State the blood parasite species.
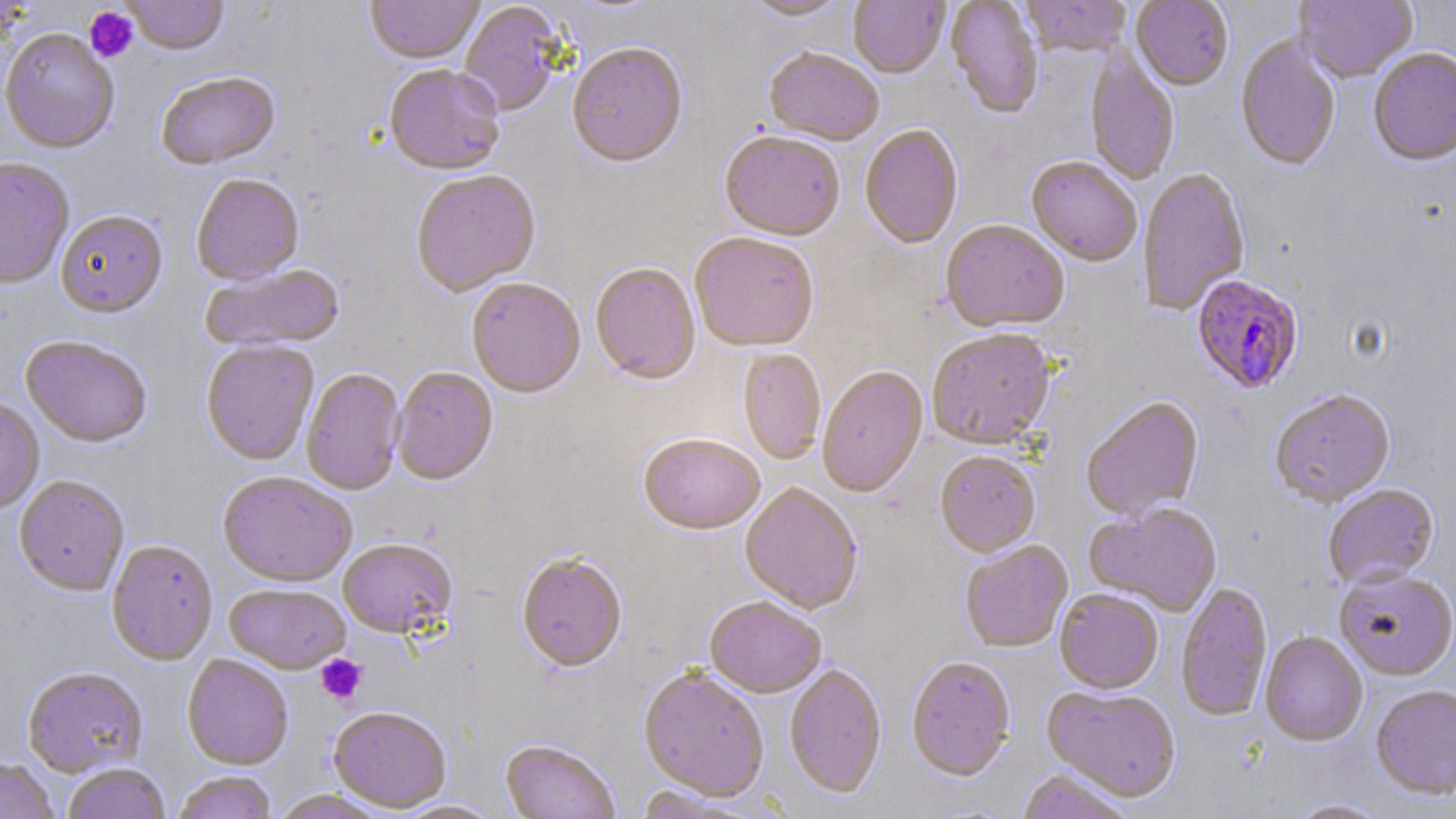
Plasmodium falciparum.

{
  "preparation": "thin blood smear",
  "modality": "optical microscopy",
  "platelet_locations": "approximate bounding boxes as (x1, y1, x2, y2) in pixels: (84, 6, 139, 63), (316, 654, 366, 705)",
  "uninfected_red_blood_cell_locations": "approximate bounding boxes as (x1, y1, x2, y2) in pixels: (122, 0, 229, 56), (365, 0, 484, 66), (741, 0, 853, 23), (849, 0, 949, 80), (945, 0, 1043, 121), (1020, 0, 1132, 59), (1131, 0, 1233, 92), (1294, 0, 1417, 85), (459, 2, 567, 118), (0, 29, 120, 155), (1236, 37, 1340, 173), (567, 45, 688, 171), (1368, 49, 1456, 169), (764, 50, 883, 148), (1086, 52, 1179, 186), (384, 66, 505, 178), (157, 74, 280, 172), (860, 125, 964, 251), (720, 134, 845, 243), (1026, 158, 1142, 268), (0, 159, 75, 291), (1137, 169, 1250, 316), (411, 171, 541, 298), (191, 175, 305, 287), (56, 212, 167, 320), (941, 221, 1069, 335), (690, 235, 818, 354), (200, 264, 347, 354), (590, 264, 701, 386), (466, 280, 585, 399), (927, 331, 1056, 451), (21, 337, 152, 449), (201, 341, 319, 467), (738, 349, 826, 464), (817, 367, 929, 499), (301, 368, 405, 497), (392, 368, 498, 486), (1270, 391, 1395, 508), (1081, 397, 1205, 522), (0, 398, 45, 515), (639, 436, 764, 537), (935, 452, 1041, 559), (217, 473, 357, 589), (14, 477, 129, 596), (740, 484, 863, 616), (1323, 485, 1439, 591), (1084, 504, 1222, 618), (106, 541, 218, 666), (338, 541, 458, 641), (960, 542, 1073, 654), (517, 556, 627, 674), (1334, 571, 1456, 682), (1176, 582, 1273, 722), (224, 584, 351, 675), (1054, 590, 1163, 696), (704, 599, 826, 699), (1260, 632, 1368, 747), (182, 656, 293, 771), (906, 658, 1015, 783), (784, 665, 887, 800), (22, 668, 148, 778), (638, 669, 769, 803), (1370, 686, 1456, 801), (1041, 687, 1181, 803), (328, 708, 451, 813), (500, 741, 620, 819), (0, 758, 60, 819), (63, 764, 170, 819), (1016, 770, 1134, 819), (172, 772, 278, 819), (631, 787, 769, 818), (271, 791, 389, 819), (1286, 798, 1395, 819), (392, 800, 505, 818)",
  "stain": "May-Grünwald-Giemsa",
  "magnification": "1000x",
  "field_of_view": "one of a larger specimen",
  "image_size": "1456×819 pixels",
  "plasmodium_falciparum_infected_red_blood_cell_locations": "approximate bounding boxes as (x1, y1, x2, y2) in pixels: (1191, 276, 1304, 396)"
}